Give the preparation type.
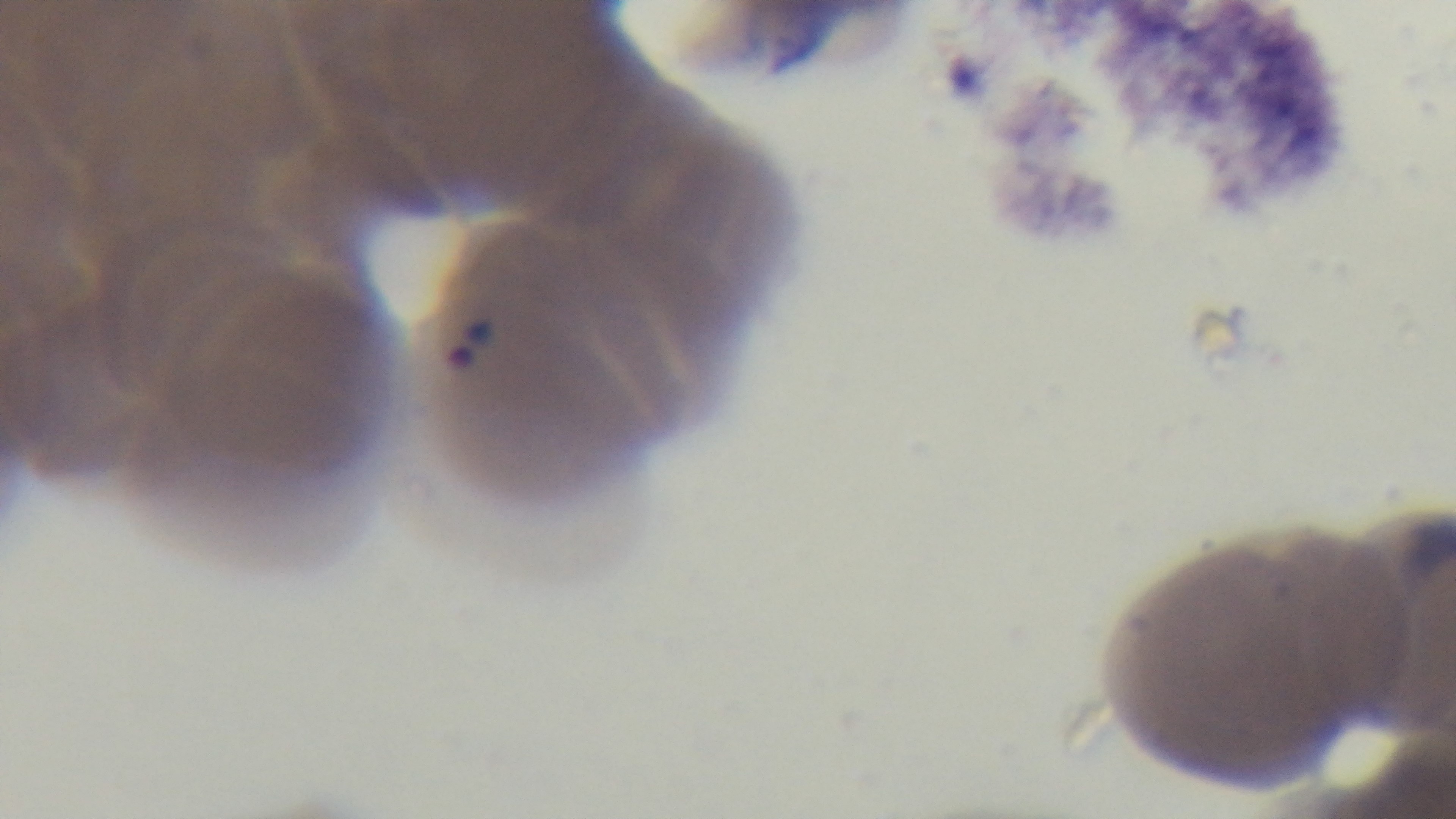
It is a thin blood film.

Light microscopy. Captured with a mounted 4K digital camera. Giemsa-stained. Single field of view. Oil-immersion objective, 100x. Malaria status: positive.